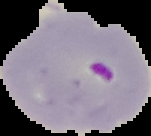
From a thin blood film. Image is 151×136 pixels. Cell region segmented out of the field of view; the surrounding area is masked to black. Malaria status: parasitized.